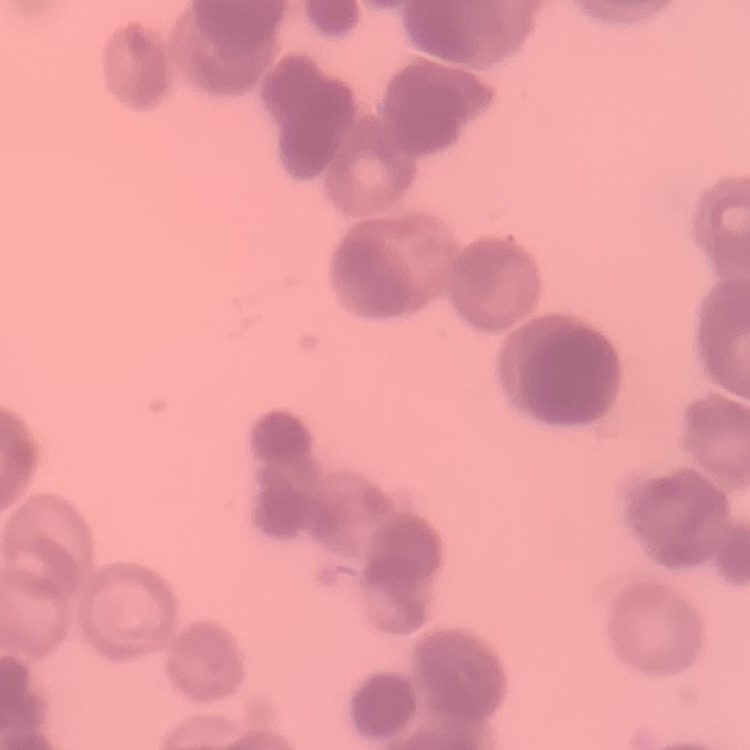

{
  "erythrocyte_morphology": "rouleaux formation",
  "preparation": "thin blood smear",
  "stain": "Field's or Giemsa",
  "image_type": "one tile cut from a larger photomicrograph"
}